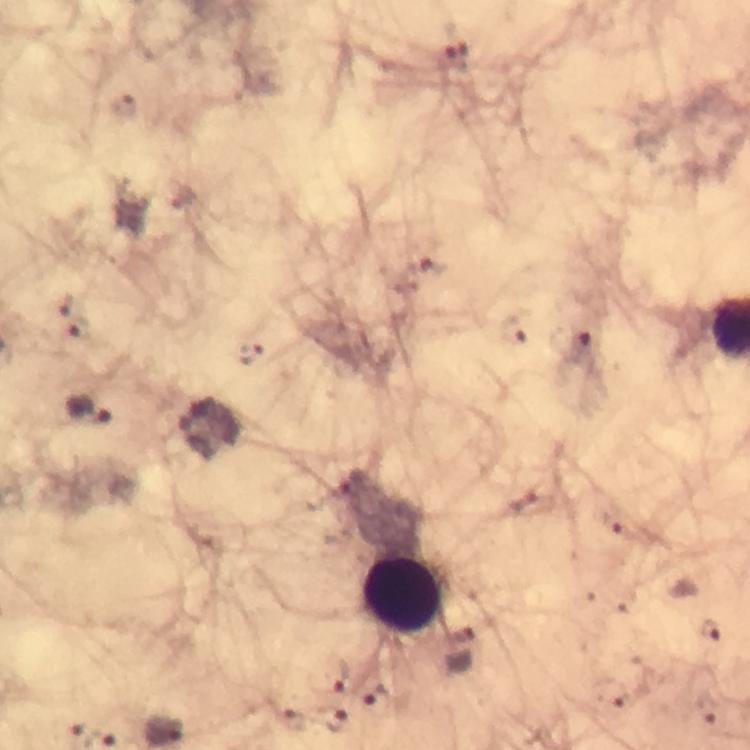
context = from a diagnostic examination for malaria
Plasmodium parasite locations = approximate object centers, in pixels from the top-left corner: (x=456, y=54), (x=431, y=268), (x=511, y=329), (x=571, y=342), (x=532, y=504), (x=714, y=629), (x=340, y=676), (x=336, y=720)
preparation = thick blood film
immersion oil = used
stain = Giemsa
magnification = 100x
capture = smartphone mounted on the microscope
cropped from = a single field of view
image size = 750×750 pixels
leukocyte locations = approximate object centers, in pixels from the top-left corner: (x=404, y=596)